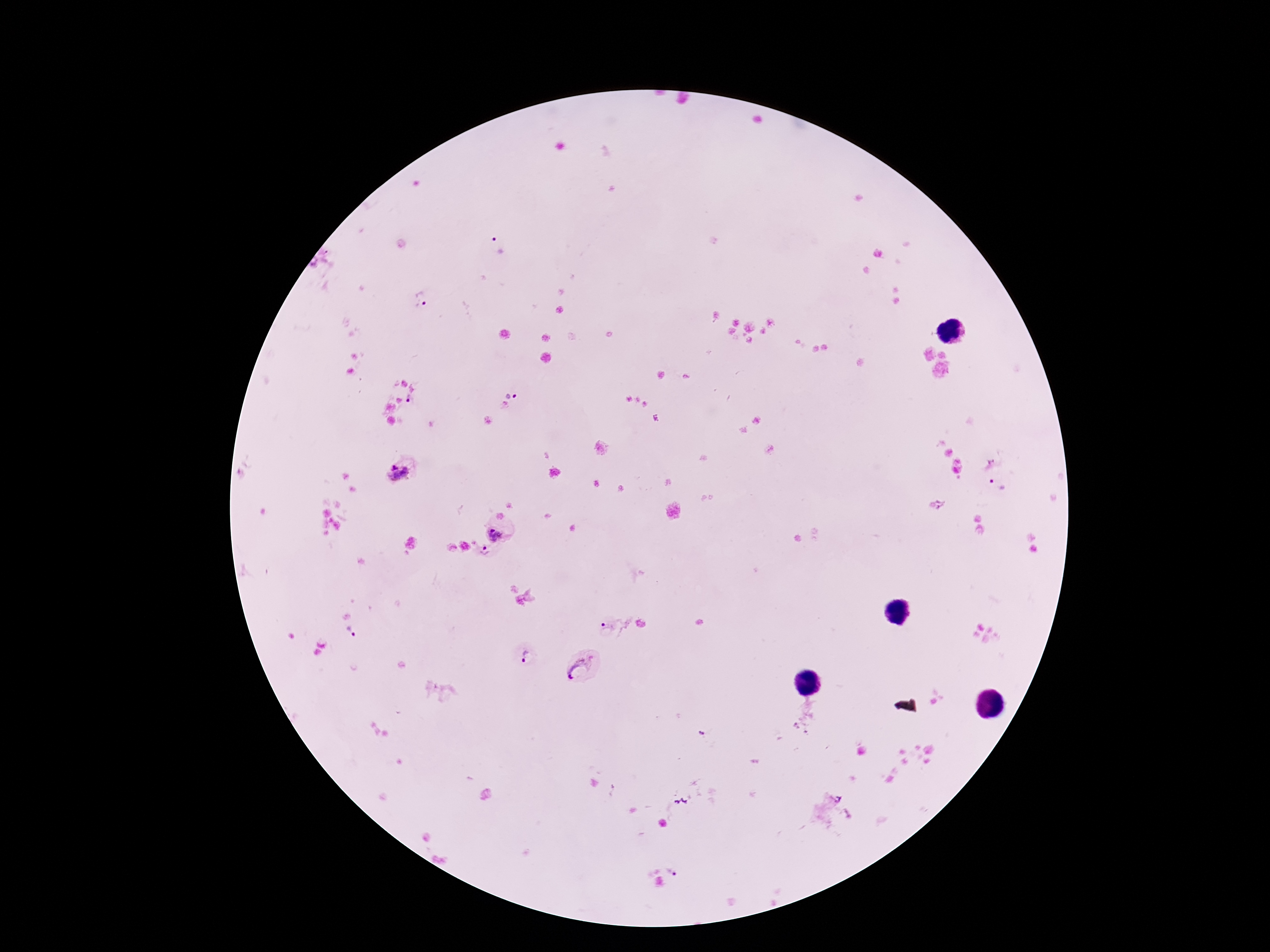

Approximate centers as [x, y] in pixels. Plasmodium parasite locations: [497, 245], [424, 303], [513, 391], [412, 403], [990, 463], [398, 473], [998, 487], [937, 504], [497, 536], [485, 553], [608, 626], [352, 633], [527, 657], [581, 669], [674, 869]. One field from this slide. Giemsa-stained preparation. Image is 1270×952 pixels. Smartphone photograph taken through the microscope eyepiece. Thick blood film. 100x magnification. Patient malaria status: infected.